Find each parasitized red blood cell.
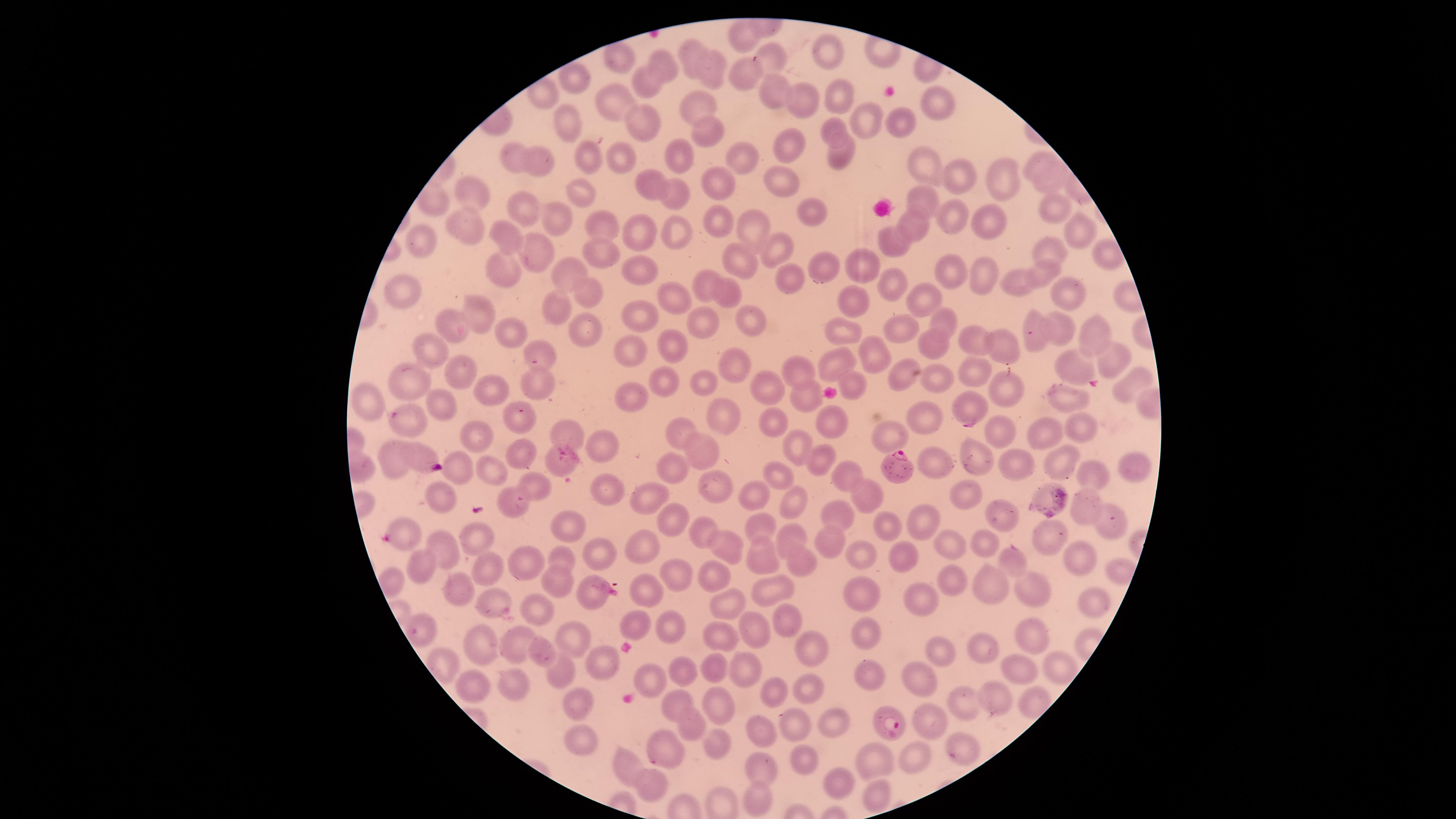

Approximate marker points as (x, y) in pixels.
Parasitized red blood cells: (896, 466), (887, 716).

field_of_view: single
species: Plasmodium falciparum
capture: smartphone photograph through the microscope eyepiece
preparation: thin blood smear
visible_region: circular
stain: Giemsa
image_size: 1456×819 pixels
uninfected_red_blood_cells: 'approximate marker points as (x, y) in pixels: (742, 33), (824, 49), (697, 52), (621, 56), (666, 60), (774, 63), (714, 65), (738, 70), (577, 82), (651, 85), (769, 87), (802, 94), (838, 94), (936, 98), (613, 105), (690, 109), (898, 117), (865, 120), (571, 123), (645, 123), (832, 126), (703, 128), (795, 143), (841, 151), (736, 154), (513, 157), (619, 157), (590, 158), (679, 158), (1036, 161), (545, 163), (922, 163), (959, 176), (1056, 178), (718, 183), (781, 183), (1005, 183), (577, 187), (654, 188), (468, 193), (676, 194), (922, 195), (1050, 206), (529, 210), (953, 213), (812, 215), (982, 217), (713, 218), (913, 221), (557, 222), (603, 222), (1077, 224), (750, 226), (467, 227), (647, 234), (676, 234), (512, 239), (894, 240), (423, 243), (780, 246), (607, 253), (1055, 254), (536, 256), (743, 262), (822, 263), (862, 266), (501, 268), (644, 269), (1042, 273), (949, 274), (571, 275), (984, 277), (787, 281), (1020, 281), (890, 284), (709, 285), (406, 288), (588, 290), (729, 290), (1069, 294), (672, 299), (922, 299), (856, 302), (553, 307), (634, 314), (478, 315), (946, 319), (752, 320), (457, 325), (706, 326), (900, 326), (583, 328), (845, 328), (1060, 329), (1032, 331), (1093, 331), (515, 336), (932, 342), (977, 343), (1004, 343), (670, 345), (436, 352), (629, 353), (873, 354), (542, 355), (1110, 355), (837, 360), (735, 367), (798, 368), (1071, 369), (980, 370), (464, 374), (412, 377), (663, 378), (937, 379), (851, 380), (542, 381), (699, 382), (1136, 383), (1011, 386), (771, 388), (499, 390), (634, 398), (805, 399), (1059, 399), (366, 402), (440, 404), (972, 407), (723, 417), (773, 418), (925, 418), (407, 421), (520, 421), (830, 421), (1084, 423), (678, 429), (474, 434), (1006, 434), (891, 435), (1042, 435), (564, 437), (800, 441), (604, 442), (710, 446), (517, 450), (816, 456), (396, 457), (419, 457), (975, 460), (934, 461), (1060, 462), (673, 464), (1009, 464), (1134, 466), (485, 468), (847, 468), (780, 474), (461, 475), (1090, 475), (529, 488), (717, 488), (612, 489), (754, 493), (964, 493), (438, 496), (647, 497), (866, 497), (793, 500), (1041, 501), (515, 503), (1083, 506), (838, 515), (1002, 518), (667, 521), (929, 522), (887, 523), (403, 525), (1113, 525), (563, 528), (766, 528), (696, 529), (794, 533), (832, 536), (476, 538), (984, 538), (1046, 539), (949, 540), (442, 542), (648, 548), (728, 550), (862, 555), (905, 556), (594, 557), (518, 558), (763, 558), (1012, 558), (560, 559), (1081, 559), (801, 562), (424, 567), (486, 571), (953, 578), (717, 579), (685, 580), (558, 581), (988, 582), (771, 587), (460, 588), (645, 589), (1033, 589), (861, 591), (591, 592), (925, 596), (1087, 600), (719, 603), (496, 605), (540, 608), (788, 614), (634, 623), (679, 625), (756, 630), (425, 631), (719, 632), (863, 634), (1031, 637), (576, 639), (480, 641), (520, 644), (982, 645), (944, 650), (813, 652), (545, 655), (1057, 663), (602, 664), (717, 668), (1022, 668), (745, 669), (684, 671), (561, 674), (870, 674), (656, 676), (920, 677), (809, 679), (777, 682), (475, 683), (518, 683), (997, 697), (969, 698), (676, 700), (579, 705), (716, 706), (687, 719), (923, 721), (800, 724), (833, 724), (761, 732), (583, 738), (720, 747), (670, 751), (916, 753), (869, 755), (800, 757), (966, 757), (625, 765), (768, 767), (839, 779), (649, 783), (874, 793), (753, 800)'